Locate every blood parasite and identify its species.
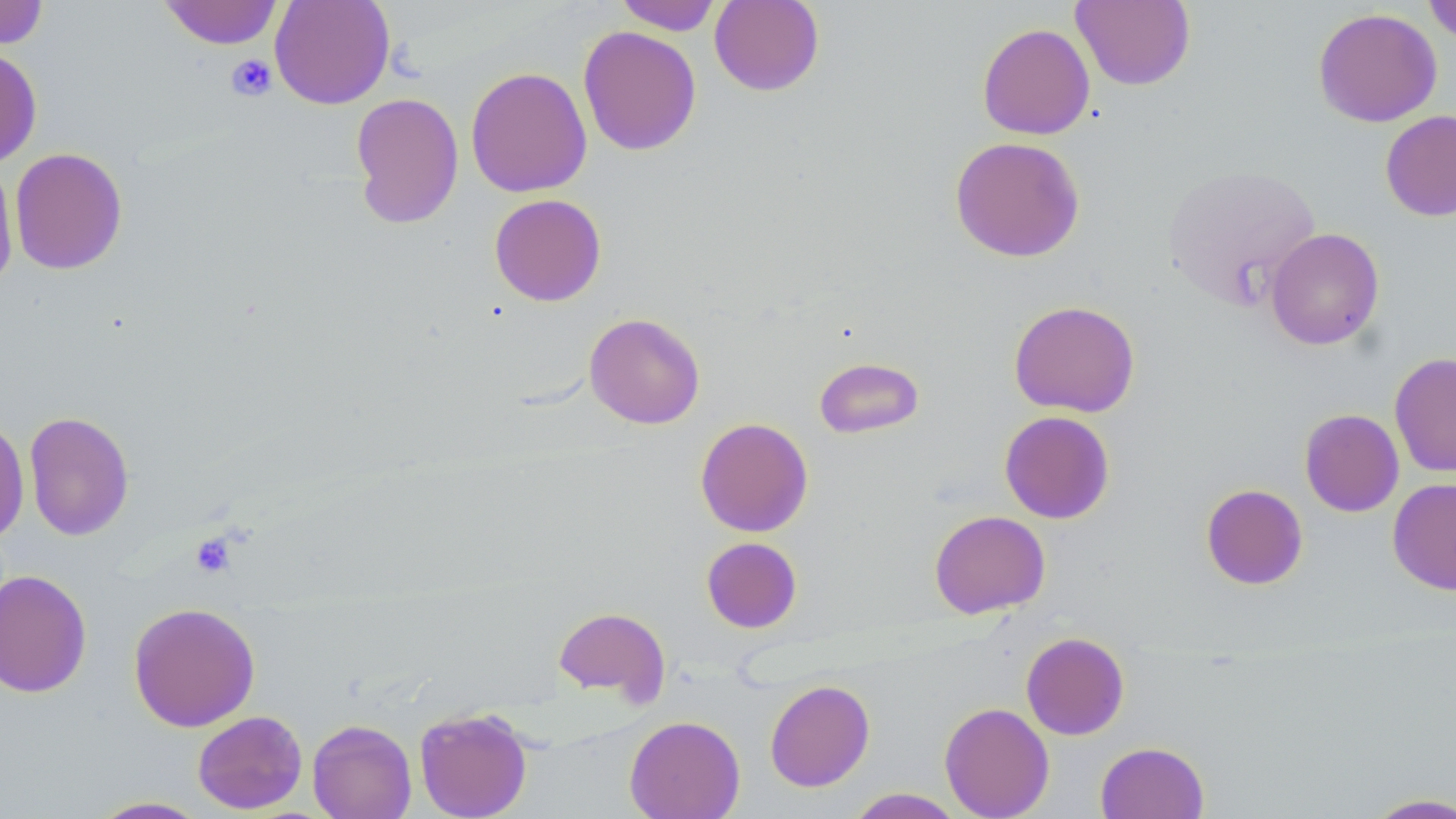

No blood parasites seen.

Summary:
  - Coordinate format: approximate bounding boxes as (x1, y1, x2, y2) in pixels
  - Platelet locations: (226, 55, 277, 101), (189, 532, 237, 578)
  - Uninfected red blood cell locations: (159, 0, 283, 50), (269, 0, 395, 109), (614, 0, 724, 35), (709, 0, 825, 96), (1071, 0, 1195, 91), (1422, 0, 1456, 44), (0, 1, 49, 49), (1313, 7, 1442, 127), (977, 23, 1095, 140), (578, 26, 702, 156), (0, 46, 42, 168), (465, 66, 592, 198), (350, 91, 464, 230), (1380, 110, 1456, 222), (949, 136, 1085, 262), (9, 147, 128, 275), (0, 156, 19, 290), (1163, 165, 1320, 309), (489, 193, 607, 306), (1265, 227, 1384, 350), (1008, 300, 1140, 417), (584, 313, 706, 429), (1389, 352, 1456, 477), (814, 357, 925, 439), (1299, 409, 1404, 517), (23, 411, 134, 541), (999, 411, 1115, 524), (0, 416, 29, 545), (695, 417, 814, 537), (1387, 477, 1456, 595), (1200, 483, 1308, 590), (928, 510, 1050, 618), (701, 537, 802, 634), (0, 569, 92, 698), (128, 601, 261, 732), (553, 605, 671, 704), (1021, 632, 1130, 740), (764, 679, 875, 792), (939, 702, 1055, 818), (414, 707, 533, 819), (192, 710, 308, 814), (625, 715, 745, 819), (307, 719, 417, 819), (1095, 741, 1209, 819), (846, 788, 966, 818), (1362, 792, 1456, 818), (87, 796, 212, 818)
  - Slide-level diagnosis: negative for blood parasites
  - Modality: light microscopy
  - Image size: 1456×819 pixels
  - Magnification: 1000x
  - Stain: May-Grünwald-Giemsa
  - Preparation: thin blood smear
  - Field of view: single